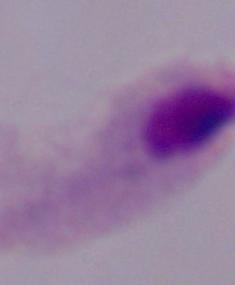

Summary:
  - Magnification: 1000x
  - Identification: trichomonad
  - Modality: micrograph